State which cell type is depicted.
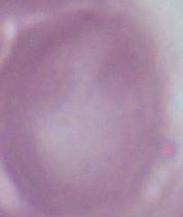

This is an erythrocyte.

modality = photomicrograph
magnification = 1000x